Classify this cell by malaria status.
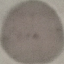
Uninfected.

{
  "capture": "smartphone camera at the microscope eyepiece",
  "stain": "Giemsa",
  "image_type": "automatically extracted cell patch, resized to 64 × 64 pixels",
  "preparation": "thin smear"
}